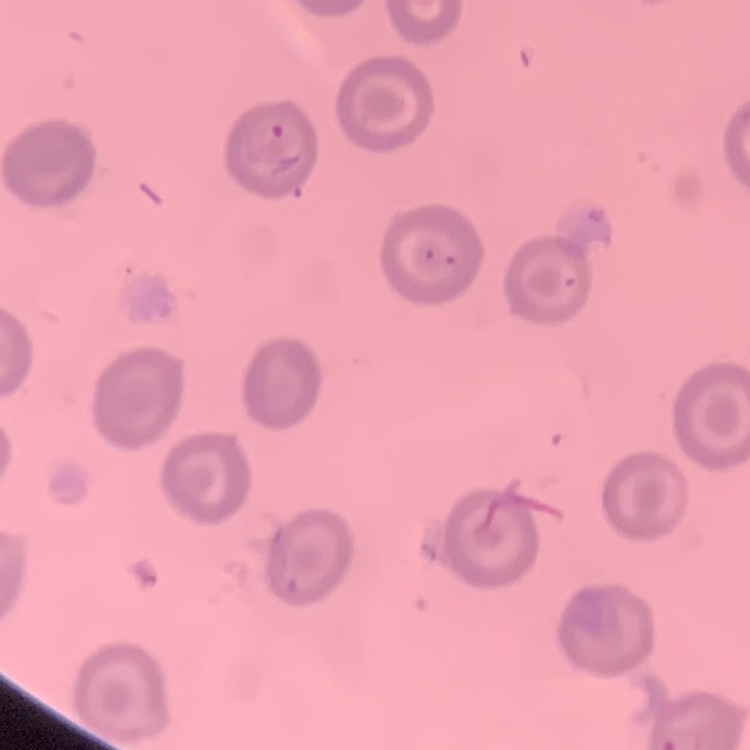
{
  "erythrocyte_morphology": "no rouleaux formation",
  "image_type": "square crop of a larger photomicrograph",
  "stain": "Field's or Giemsa",
  "preparation": "thin blood smear"
}